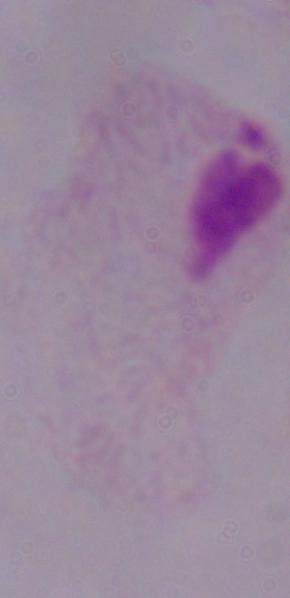

Photomicrograph. A trichomonad is shown. 1000x magnification.